Locate every Plasmodium parasite and every leukocyte.
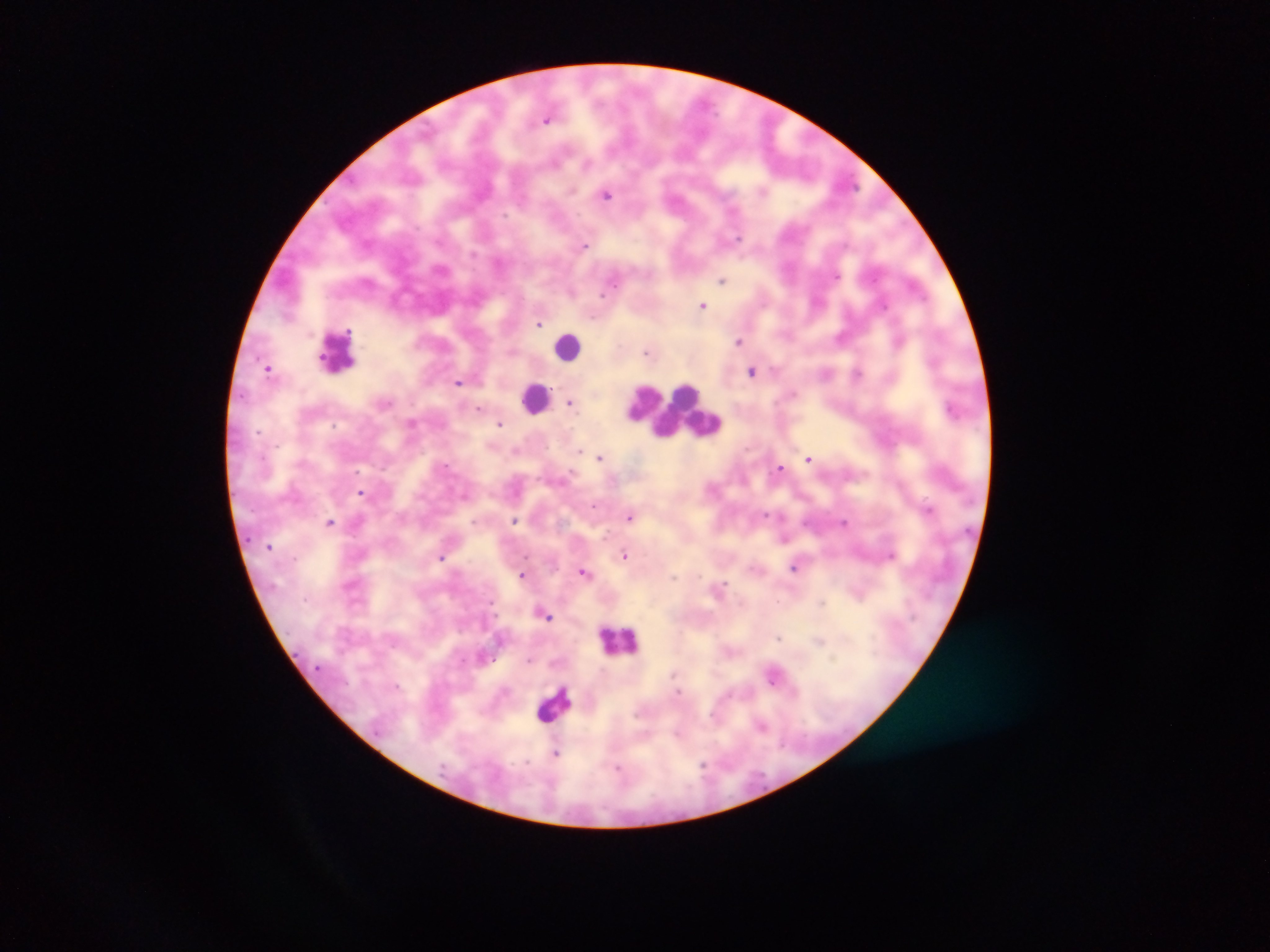
Approximate centers as {x, y} in pixels.
Plasmodium parasites: {547, 118}, {607, 193}, {584, 245}, {723, 279}, {703, 305}, {539, 323}, {900, 339}, {740, 341}, {648, 352}, {268, 368}, {752, 370}, {858, 373}, {458, 382}, {570, 402}, {480, 407}, {953, 408}, {412, 422}, {500, 423}, {581, 450}, {601, 457}, {809, 458}, {780, 467}, {361, 492}, {593, 504}, {929, 509}, {765, 514}, {631, 515}, {514, 520}, {330, 522}, {845, 523}, {784, 538}, {624, 554}, {441, 558}, {796, 566}, {585, 572}, {522, 574}, {719, 587}, {545, 613}, {780, 637}, {819, 640}, {530, 660}, {774, 674}, {762, 725}, {556, 752}.
Leukocytes: {568, 344}, {338, 350}, {534, 398}, {675, 408}, {620, 638}, {554, 705}.

image size = 1270×952 pixels
country = Ghana
preparation = thick blood smear
capture = mobile-phone photograph through a microscope
field of view = single